Report the malaria status of this cell.
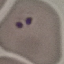
It is parasitized.

Thin blood film. Photographed with a smartphone camera at the microscope eyepiece. Giemsa-stained preparation. Automatically extracted cell patch, resized to 64 × 64 pixels.